State the preparation type.
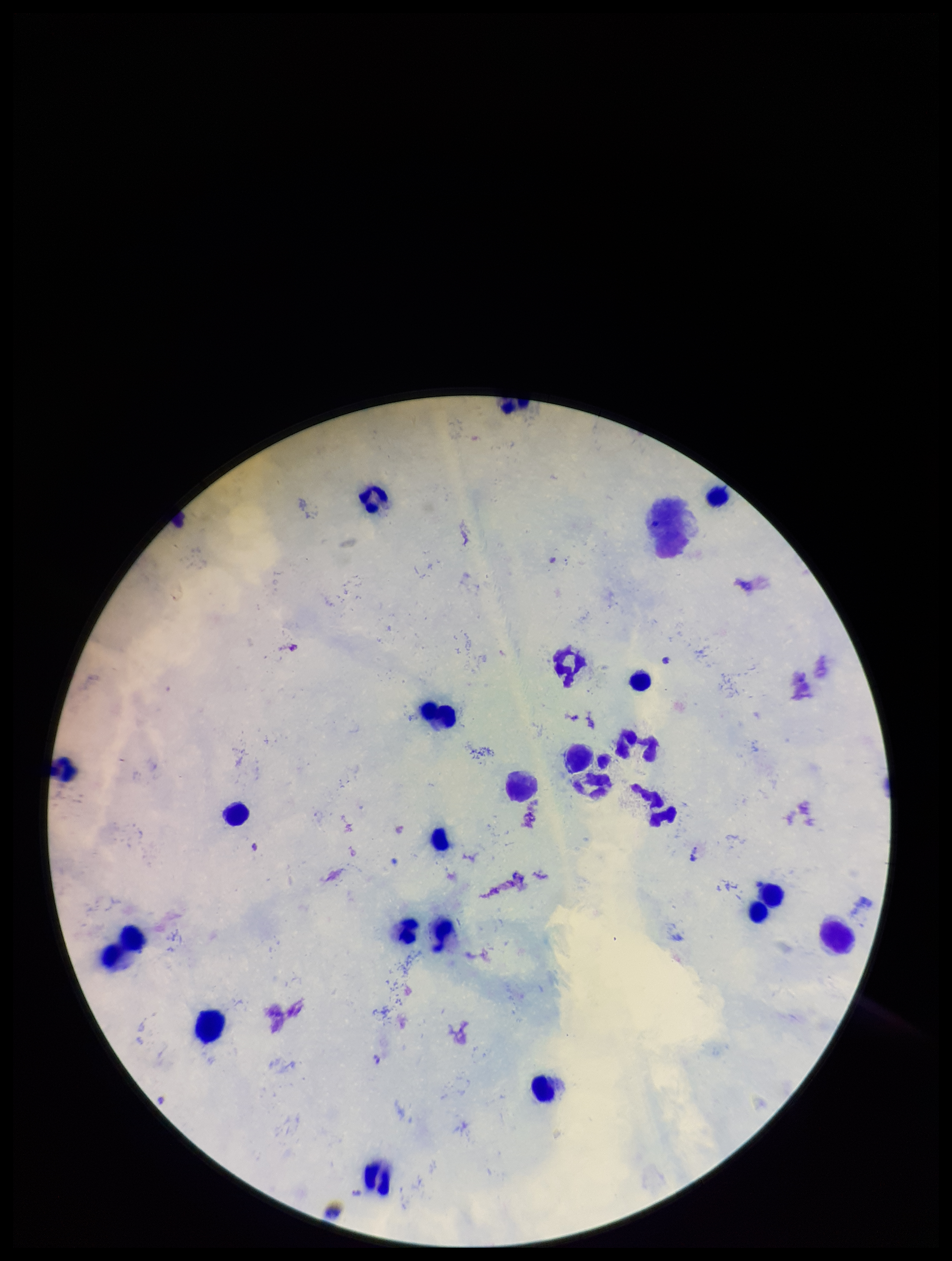

A thick smear.

Giemsa stain. Plasmodium parasites: none identified. Image is 952×1261 pixels. Parasite count: 0. Leukocyte count: 22. Patient malaria status: positive. Species reported for this patient: Plasmodium falciparum. Smartphone photograph taken through the eyepiece of a microscope. One field from this slide.